Identify the parasite.
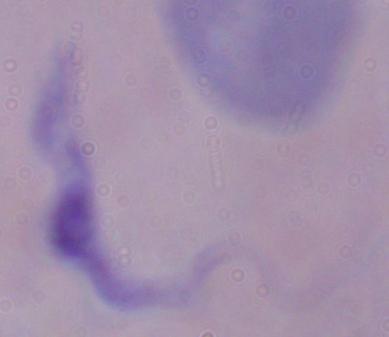

A trypanosome.

1000x magnification. Photomicrograph.